Outline each blood parasite and name the species.
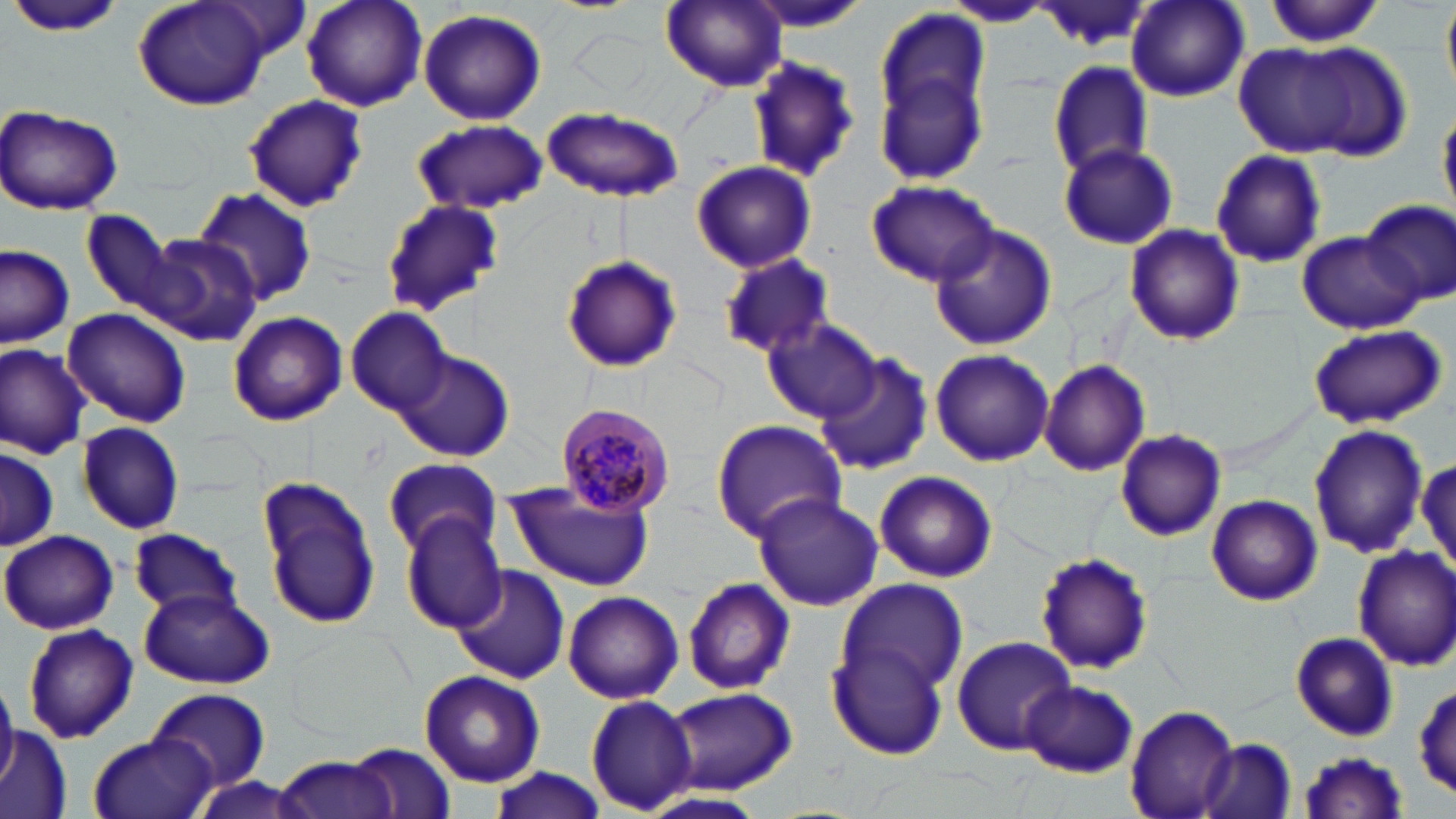
Approximate bounding boxes as named x1/y1/x2/y2 corners in pixels.
Plasmodium malariae-infected red blood cells: (x1=555, y1=401, x2=676, y2=519).
No Plasmodium falciparum, Plasmodium ovale, Plasmodium vivax, Babesia divergens, or Trypanosoma brucei observed.

slide_level_diagnosis: Plasmodium malariae
preparation: thin blood smear
modality: optical microscopy
image_size: 1456×819 pixels
field_of_view: single
magnification: 1000x
uninfected_red_blood_cell_locations: 'approximate bounding boxes as named x1/y1/x2/y2 corners in pixels: (x1=134, y1=0, x2=271, y2=110), (x1=299, y1=0, x2=429, y2=114), (x1=661, y1=0, x2=787, y2=91), (x1=742, y1=0, x2=874, y2=32), (x1=1264, y1=0, x2=1383, y2=49), (x1=944, y1=2, x2=1051, y2=29), (x1=1033, y1=2, x2=1155, y2=52), (x1=1126, y1=2, x2=1250, y2=104), (x1=9, y1=3, x2=127, y2=39), (x1=1441, y1=3, x2=1455, y2=99), (x1=417, y1=9, x2=548, y2=126), (x1=874, y1=13, x2=990, y2=184), (x1=1241, y1=38, x2=1405, y2=160), (x1=746, y1=55, x2=862, y2=183), (x1=1048, y1=61, x2=1154, y2=179), (x1=242, y1=95, x2=367, y2=212), (x1=1, y1=103, x2=126, y2=215), (x1=541, y1=105, x2=684, y2=205), (x1=1438, y1=110, x2=1455, y2=214), (x1=411, y1=119, x2=549, y2=216), (x1=1059, y1=140, x2=1180, y2=251), (x1=1210, y1=149, x2=1326, y2=266), (x1=691, y1=160, x2=816, y2=274), (x1=866, y1=180, x2=998, y2=288), (x1=193, y1=187, x2=319, y2=308), (x1=381, y1=198, x2=502, y2=316), (x1=1360, y1=202, x2=1455, y2=307), (x1=81, y1=211, x2=176, y2=313), (x1=927, y1=224, x2=1057, y2=349), (x1=1123, y1=224, x2=1246, y2=347), (x1=1297, y1=232, x2=1420, y2=334), (x1=142, y1=235, x2=262, y2=346), (x1=0, y1=244, x2=76, y2=347), (x1=561, y1=253, x2=682, y2=372), (x1=720, y1=253, x2=837, y2=361), (x1=62, y1=307, x2=191, y2=428), (x1=346, y1=309, x2=454, y2=417), (x1=227, y1=311, x2=348, y2=427), (x1=763, y1=321, x2=882, y2=424), (x1=1308, y1=323, x2=1445, y2=430), (x1=0, y1=342, x2=92, y2=458), (x1=930, y1=348, x2=1055, y2=465), (x1=816, y1=350, x2=934, y2=473), (x1=395, y1=351, x2=515, y2=464), (x1=1038, y1=359, x2=1151, y2=477), (x1=76, y1=421, x2=184, y2=534), (x1=710, y1=421, x2=847, y2=541), (x1=1309, y1=425, x2=1430, y2=557), (x1=1115, y1=428, x2=1227, y2=542), (x1=0, y1=445, x2=60, y2=553), (x1=381, y1=456, x2=501, y2=559), (x1=1416, y1=459, x2=1454, y2=574), (x1=875, y1=470, x2=997, y2=582), (x1=259, y1=476, x2=380, y2=630), (x1=505, y1=485, x2=658, y2=593), (x1=751, y1=492, x2=883, y2=610), (x1=1207, y1=495, x2=1321, y2=604), (x1=401, y1=513, x2=508, y2=631), (x1=129, y1=527, x2=242, y2=619), (x1=1, y1=530, x2=117, y2=634), (x1=1353, y1=545, x2=1456, y2=670), (x1=1035, y1=551, x2=1155, y2=675), (x1=450, y1=565, x2=571, y2=685), (x1=682, y1=577, x2=796, y2=693), (x1=836, y1=579, x2=968, y2=698), (x1=140, y1=587, x2=274, y2=689), (x1=563, y1=590, x2=683, y2=705), (x1=21, y1=625, x2=139, y2=743), (x1=1291, y1=633, x2=1399, y2=741), (x1=949, y1=635, x2=1076, y2=756), (x1=826, y1=641, x2=948, y2=760), (x1=419, y1=669, x2=545, y2=787), (x1=1020, y1=680, x2=1139, y2=776), (x1=0, y1=683, x2=18, y2=788), (x1=1412, y1=685, x2=1455, y2=801), (x1=661, y1=687, x2=800, y2=792), (x1=146, y1=689, x2=271, y2=795), (x1=585, y1=695, x2=699, y2=814), (x1=1124, y1=703, x2=1240, y2=819), (x1=1, y1=724, x2=71, y2=819), (x1=88, y1=733, x2=213, y2=819), (x1=1198, y1=737, x2=1297, y2=819), (x1=351, y1=743, x2=457, y2=819), (x1=1296, y1=750, x2=1411, y2=818), (x1=276, y1=751, x2=400, y2=819), (x1=485, y1=766, x2=614, y2=819)'
stain: May-Grünwald-Giemsa